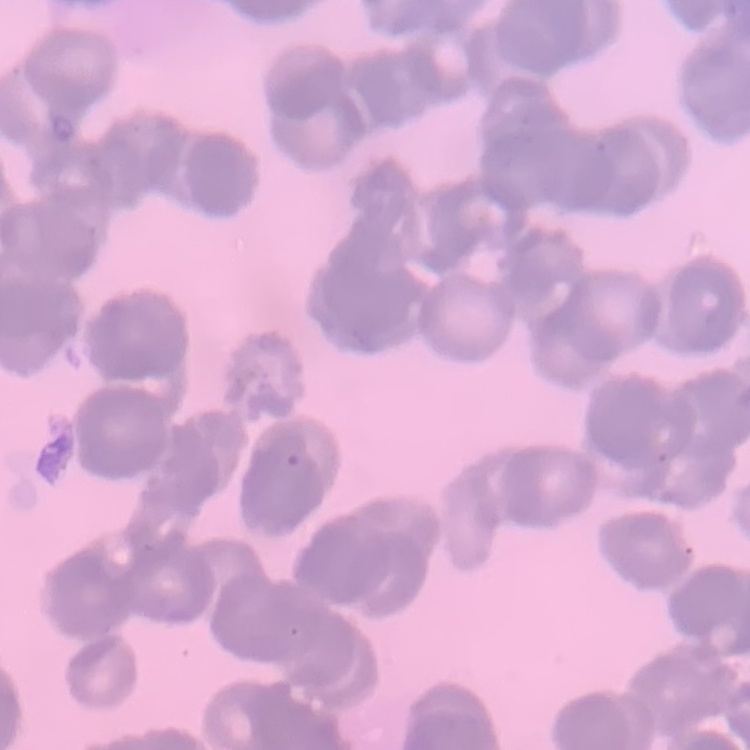

red_blood_cell_morphology: rouleaux formation
stain: Field's or Giemsa
image_type: square crop of a larger photomicrograph
preparation: thin blood film